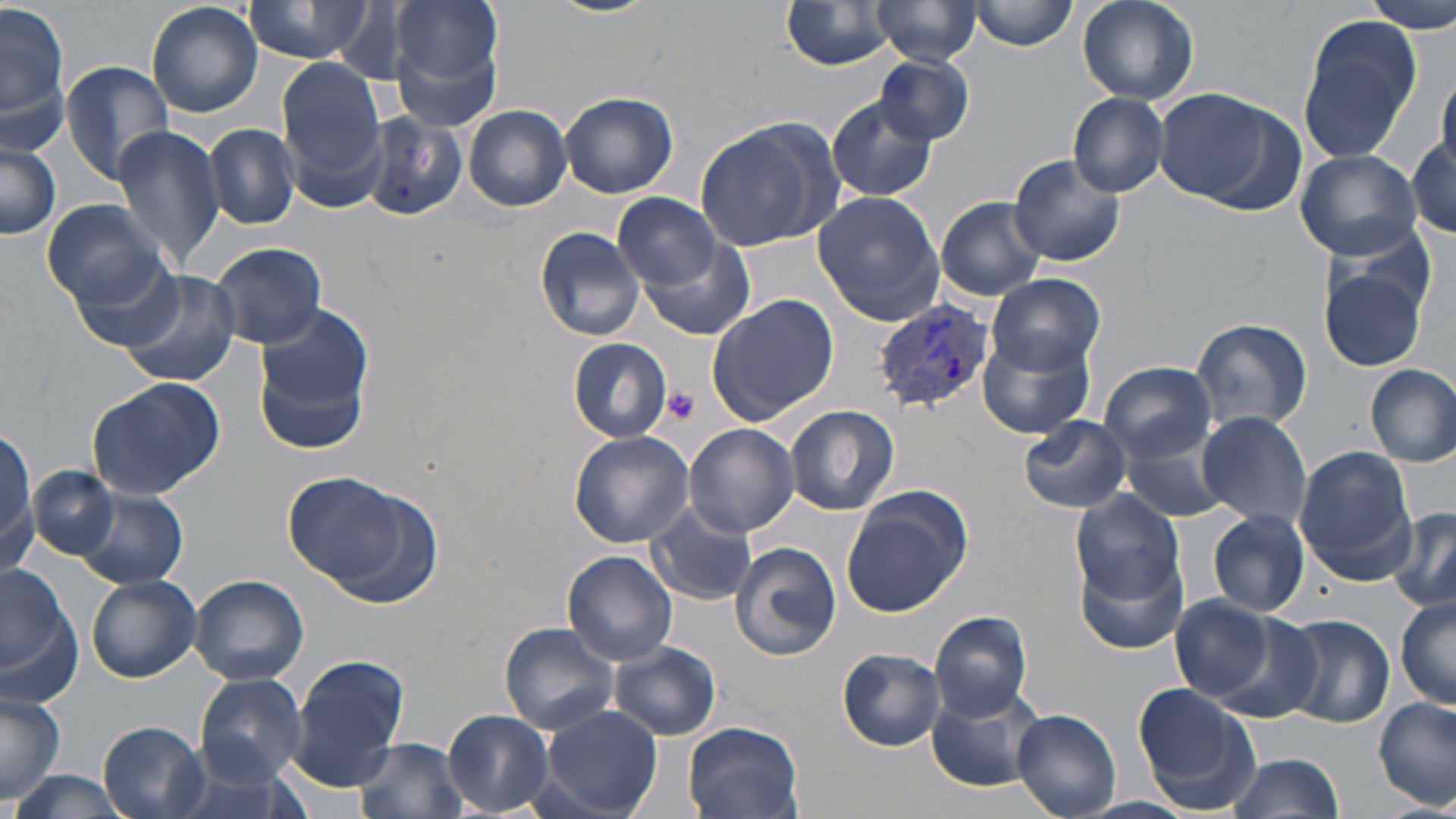
Approximate bounding boxes as named x1/y1/x2/y2 corners in pixels. Platelet locations: (x1=661, y1=387, x2=698, y2=422). Plasmodium vivax-infected red blood cell locations: (x1=874, y1=299, x2=992, y2=414). Uninfected red blood cell locations: (x1=2, y1=0, x2=70, y2=145), (x1=245, y1=0, x2=370, y2=64), (x1=388, y1=0, x2=503, y2=99), (x1=548, y1=0, x2=660, y2=17), (x1=870, y1=0, x2=984, y2=65), (x1=1076, y1=0, x2=1197, y2=105), (x1=1361, y1=0, x2=1456, y2=33), (x1=146, y1=1, x2=264, y2=118), (x1=968, y1=1, x2=1078, y2=51), (x1=782, y1=2, x2=900, y2=70), (x1=1296, y1=12, x2=1424, y2=161), (x1=873, y1=54, x2=974, y2=145), (x1=278, y1=57, x2=389, y2=202), (x1=61, y1=62, x2=174, y2=189), (x1=1435, y1=71, x2=1455, y2=182), (x1=1153, y1=90, x2=1287, y2=206), (x1=557, y1=92, x2=679, y2=200), (x1=1068, y1=92, x2=1169, y2=198), (x1=826, y1=97, x2=939, y2=203), (x1=463, y1=104, x2=571, y2=212), (x1=361, y1=111, x2=468, y2=223), (x1=694, y1=115, x2=842, y2=253), (x1=206, y1=124, x2=299, y2=230), (x1=112, y1=126, x2=227, y2=273), (x1=1410, y1=131, x2=1455, y2=237), (x1=0, y1=138, x2=60, y2=239), (x1=1294, y1=148, x2=1423, y2=260), (x1=1007, y1=154, x2=1127, y2=268), (x1=614, y1=192, x2=721, y2=287), (x1=812, y1=192, x2=945, y2=322), (x1=934, y1=196, x2=1049, y2=301), (x1=42, y1=198, x2=168, y2=308), (x1=534, y1=226, x2=646, y2=341), (x1=632, y1=230, x2=756, y2=341), (x1=209, y1=242, x2=328, y2=349), (x1=66, y1=253, x2=186, y2=352), (x1=1316, y1=261, x2=1430, y2=374), (x1=116, y1=267, x2=241, y2=389), (x1=989, y1=274, x2=1104, y2=373), (x1=708, y1=294, x2=841, y2=423), (x1=254, y1=304, x2=372, y2=452), (x1=1191, y1=318, x2=1312, y2=431), (x1=978, y1=327, x2=1094, y2=438), (x1=568, y1=339, x2=672, y2=442), (x1=1100, y1=363, x2=1218, y2=463), (x1=1365, y1=363, x2=1455, y2=466), (x1=84, y1=374, x2=225, y2=500), (x1=785, y1=404, x2=899, y2=514), (x1=1195, y1=413, x2=1312, y2=531), (x1=1020, y1=416, x2=1130, y2=513), (x1=683, y1=424, x2=798, y2=536), (x1=1117, y1=424, x2=1239, y2=523), (x1=0, y1=425, x2=36, y2=576), (x1=568, y1=429, x2=693, y2=548), (x1=1293, y1=447, x2=1419, y2=580), (x1=28, y1=465, x2=118, y2=559), (x1=281, y1=469, x2=434, y2=599), (x1=74, y1=487, x2=186, y2=589), (x1=1070, y1=489, x2=1183, y2=604), (x1=841, y1=491, x2=970, y2=616), (x1=646, y1=500, x2=759, y2=607), (x1=1389, y1=507, x2=1456, y2=615), (x1=1208, y1=510, x2=1311, y2=619), (x1=731, y1=542, x2=840, y2=661), (x1=1074, y1=548, x2=1189, y2=656), (x1=563, y1=550, x2=679, y2=664), (x1=0, y1=560, x2=78, y2=705), (x1=87, y1=574, x2=202, y2=682), (x1=189, y1=574, x2=309, y2=685), (x1=1170, y1=594, x2=1280, y2=703), (x1=1394, y1=596, x2=1456, y2=713), (x1=928, y1=611, x2=1035, y2=719), (x1=1279, y1=612, x2=1395, y2=728), (x1=499, y1=622, x2=621, y2=734), (x1=608, y1=641, x2=722, y2=740), (x1=839, y1=649, x2=945, y2=749), (x1=292, y1=656, x2=410, y2=791), (x1=194, y1=673, x2=307, y2=784), (x1=926, y1=681, x2=1053, y2=793), (x1=1133, y1=685, x2=1263, y2=814), (x1=0, y1=692, x2=66, y2=802), (x1=1375, y1=696, x2=1455, y2=811), (x1=539, y1=705, x2=664, y2=818), (x1=443, y1=709, x2=554, y2=814), (x1=1013, y1=709, x2=1121, y2=817), (x1=99, y1=720, x2=211, y2=819), (x1=682, y1=721, x2=804, y2=819), (x1=355, y1=736, x2=470, y2=819), (x1=1229, y1=750, x2=1346, y2=819), (x1=13, y1=769, x2=135, y2=817), (x1=1080, y1=795, x2=1196, y2=817). Slide-level diagnosis: Plasmodium vivax. Optical microscopy. May-Grünwald-Giemsa stain. One field of a larger specimen. Thin blood smear. 1000x magnification. Image is 1456×819 pixels.